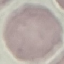 Result: no malaria parasites seen. Giemsa stain. Automatically extracted cell patch, resized to 64 × 64 pixels. Photographed with a smartphone camera at the microscope eyepiece. Thin smear of blood.